Report the malaria status of this cell.
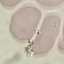

It is uninfected.

Summary:
  - Capture: smartphone camera at the microscope eyepiece
  - Image type: cell patch, automatically extracted from a larger field of view and resized to 64 × 64 pixels
  - Stain: Giemsa
  - Preparation: thin blood film